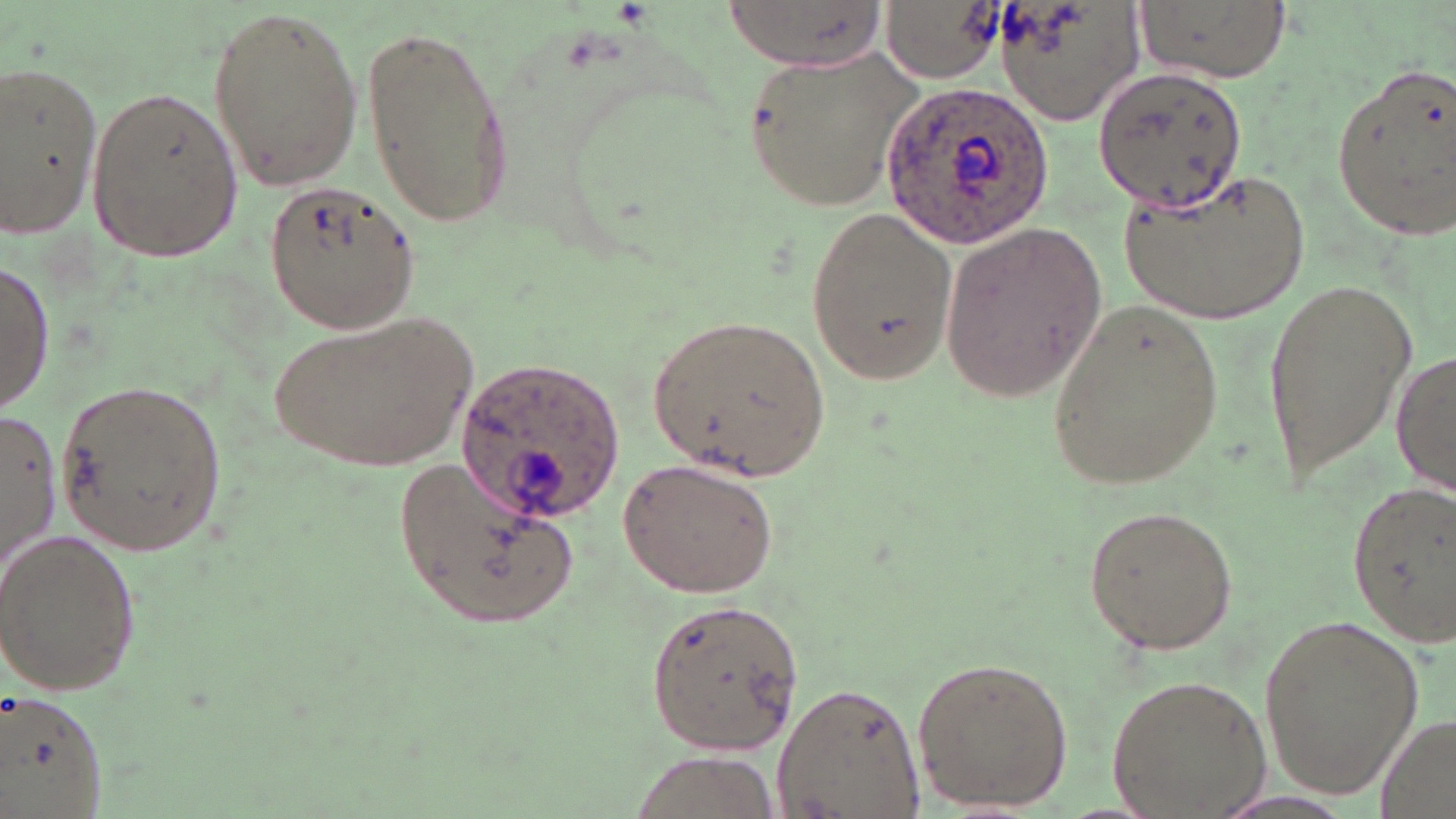

Approximate bounding boxes as named x1/y1/x2/y2 corners in pixels. Uninfected red blood cell locations: (x1=719, y1=0, x2=891, y2=66), (x1=991, y1=0, x2=1145, y2=128), (x1=1138, y1=0, x2=1287, y2=82), (x1=883, y1=1, x2=999, y2=82), (x1=208, y1=2, x2=363, y2=192), (x1=361, y1=22, x2=516, y2=229), (x1=743, y1=48, x2=927, y2=216), (x1=0, y1=61, x2=105, y2=238), (x1=1329, y1=61, x2=1456, y2=243), (x1=1090, y1=67, x2=1248, y2=215), (x1=84, y1=84, x2=243, y2=265), (x1=1119, y1=171, x2=1314, y2=322), (x1=262, y1=180, x2=420, y2=335), (x1=803, y1=203, x2=958, y2=384), (x1=938, y1=219, x2=1106, y2=402), (x1=0, y1=259, x2=52, y2=415), (x1=1262, y1=271, x2=1420, y2=492), (x1=1047, y1=297, x2=1224, y2=491), (x1=272, y1=310, x2=475, y2=476), (x1=646, y1=312, x2=832, y2=484), (x1=1393, y1=341, x2=1456, y2=501), (x1=52, y1=378, x2=231, y2=558), (x1=0, y1=409, x2=61, y2=577), (x1=397, y1=455, x2=583, y2=627), (x1=619, y1=456, x2=780, y2=598), (x1=1342, y1=479, x2=1455, y2=648), (x1=1080, y1=504, x2=1243, y2=658), (x1=0, y1=527, x2=142, y2=697), (x1=643, y1=597, x2=806, y2=755), (x1=1253, y1=609, x2=1426, y2=805), (x1=911, y1=653, x2=1074, y2=811), (x1=1104, y1=675, x2=1272, y2=816), (x1=770, y1=680, x2=928, y2=819), (x1=0, y1=688, x2=111, y2=817), (x1=1372, y1=712, x2=1456, y2=819), (x1=623, y1=748, x2=787, y2=818). Plasmodium ovale-infected red blood cell locations: (x1=877, y1=79, x2=1051, y2=249), (x1=457, y1=354, x2=623, y2=528). Slide-level diagnosis: Plasmodium ovale. Light microscopy. May-Grünwald-Giemsa-stained preparation. Captured at 1000x magnification. Image is 1456×819 pixels. Single field of view. Thin blood smear.